Name the parasite shown.
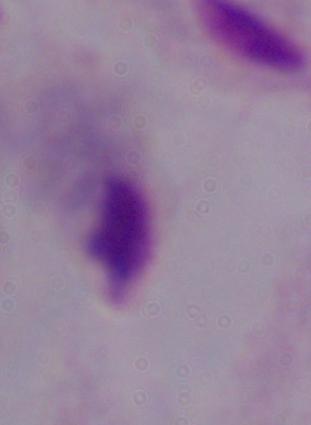
A trichomonad.

Summary:
  - Modality: photomicrograph
  - Magnification: 1000x